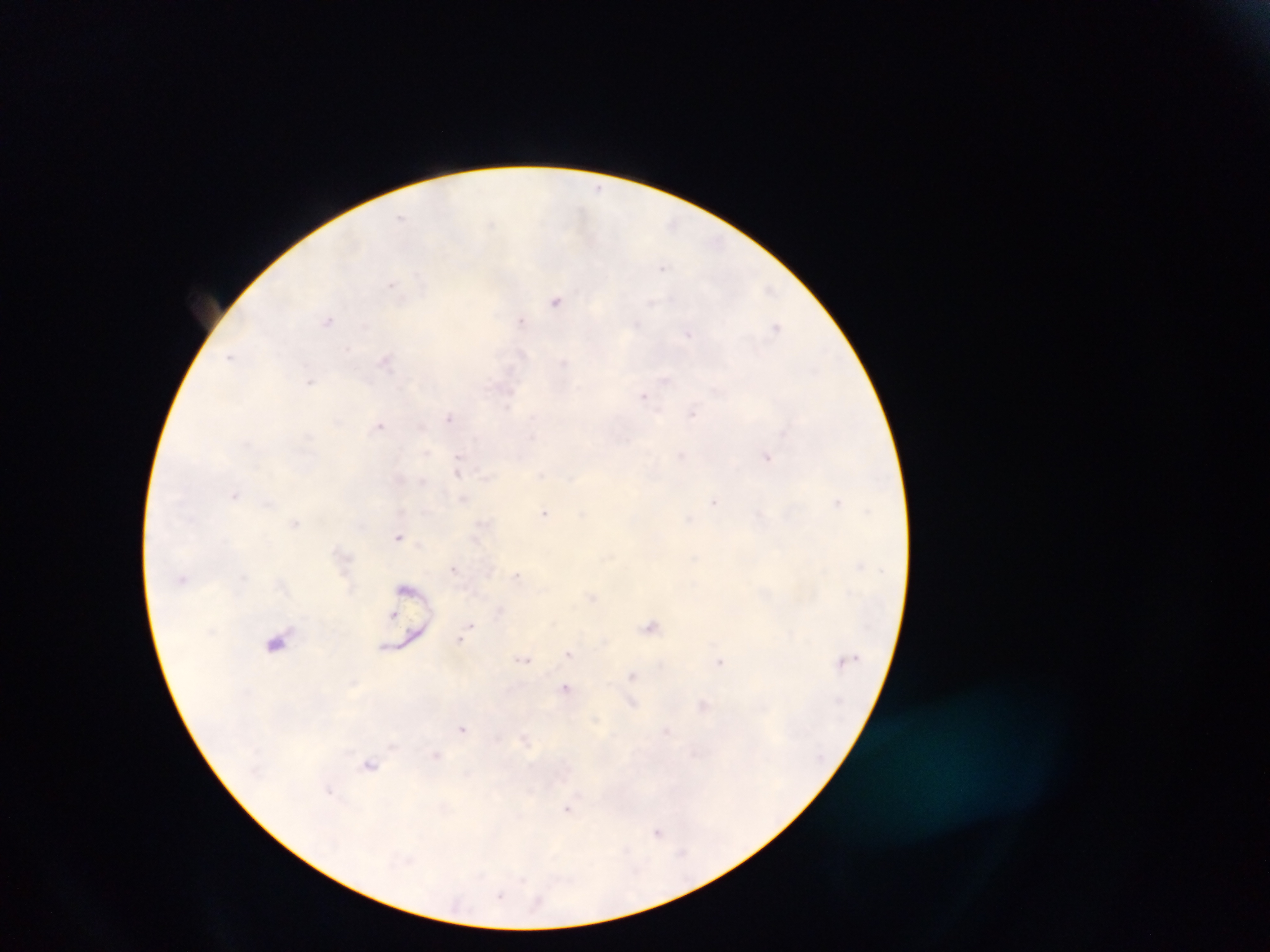

Approximate centers as [x, y] in pixels.
Summary:
  - Leukocyte locations: [276, 641]
  - Malaria parasite locations: [402, 218], [557, 299], [328, 320], [521, 321], [776, 328], [688, 333], [231, 357], [386, 360], [311, 380], [644, 395], [693, 413], [449, 418], [380, 426], [681, 455], [767, 455], [458, 468], [235, 494], [464, 499], [714, 502], [837, 502], [545, 512], [295, 523], [400, 536], [454, 568], [519, 577], [592, 597], [392, 612], [652, 626], [461, 638], [569, 653], [524, 659], [720, 662], [632, 677], [566, 688], [631, 703], [704, 705], [463, 728], [667, 733], [436, 756], [370, 764], [330, 789], [568, 808], [658, 832]
  - Preparation: thick blood smear
  - Capture: mobile-phone photograph through a microscope
  - Image size: 1270×952 pixels
  - Country: Ghana
  - Field of view: single